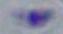
1000x magnification. Toxoplasma gondii is seen. Micrograph.